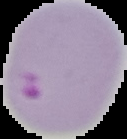

Summary:
  - Preparation: thin blood smear
  - Image type: segmented cell region with the area outside set to black
  - Result: malaria parasites detected
  - Image size: 127×139 pixels